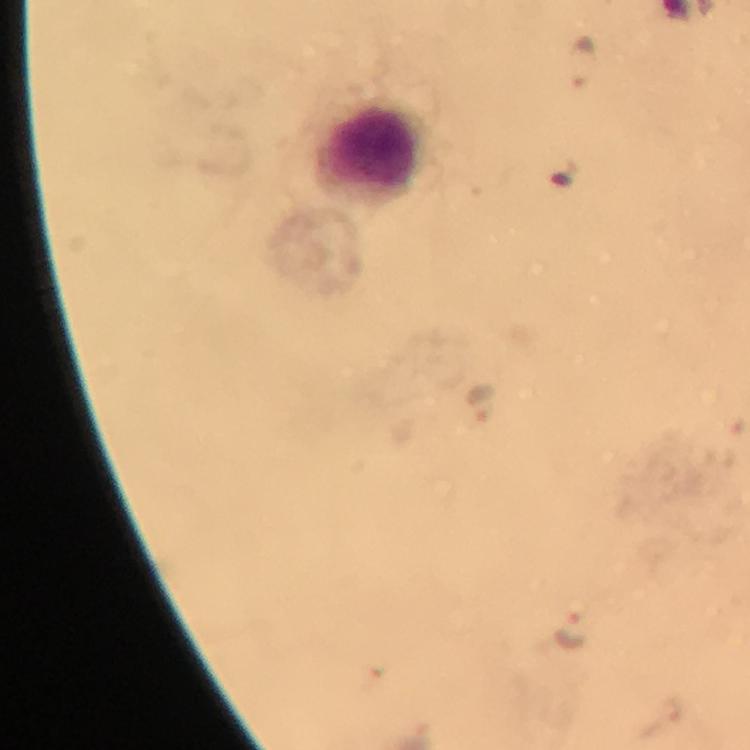
Approximate centers as [x, y] in pixels.
Summary:
  - Leukocyte locations: [372, 149]
  - Malaria parasite locations: [585, 58], [482, 401], [570, 631], [670, 709]
  - Cropped from: a single field of view
  - Capture: smartphone mounted on the microscope
  - Magnification: 100x
  - Context: from a diagnostic examination for malaria
  - Immersion oil: used
  - Image size: 750×750 pixels
  - Stain: Giemsa
  - Preparation: thick smear